Assess this cell for malaria.
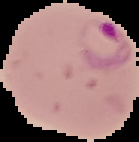
Parasitized.

Summary:
  - Image type: cell region segmented out of the field of view; surrounding area masked to black
  - Image size: 139×142 pixels
  - Preparation: thin blood film